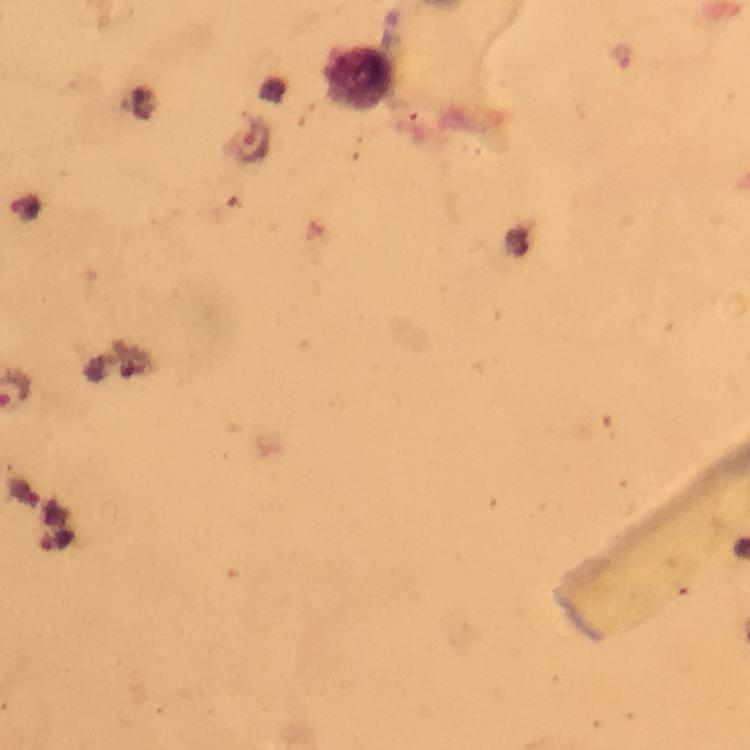

Approximate centers as [x, y] in pixels. Malaria parasite locations: [252, 143]. Leukocyte locations: [362, 80]. Image is 750×750 pixels. Cropped region of a single field of view. Thick smear. Immersion oil applied. Giemsa stain. At 100x magnification. Photographed through the microscope with a smartphone camera. From a malaria diagnostic workup.